Outline each uninfected red blood cell.
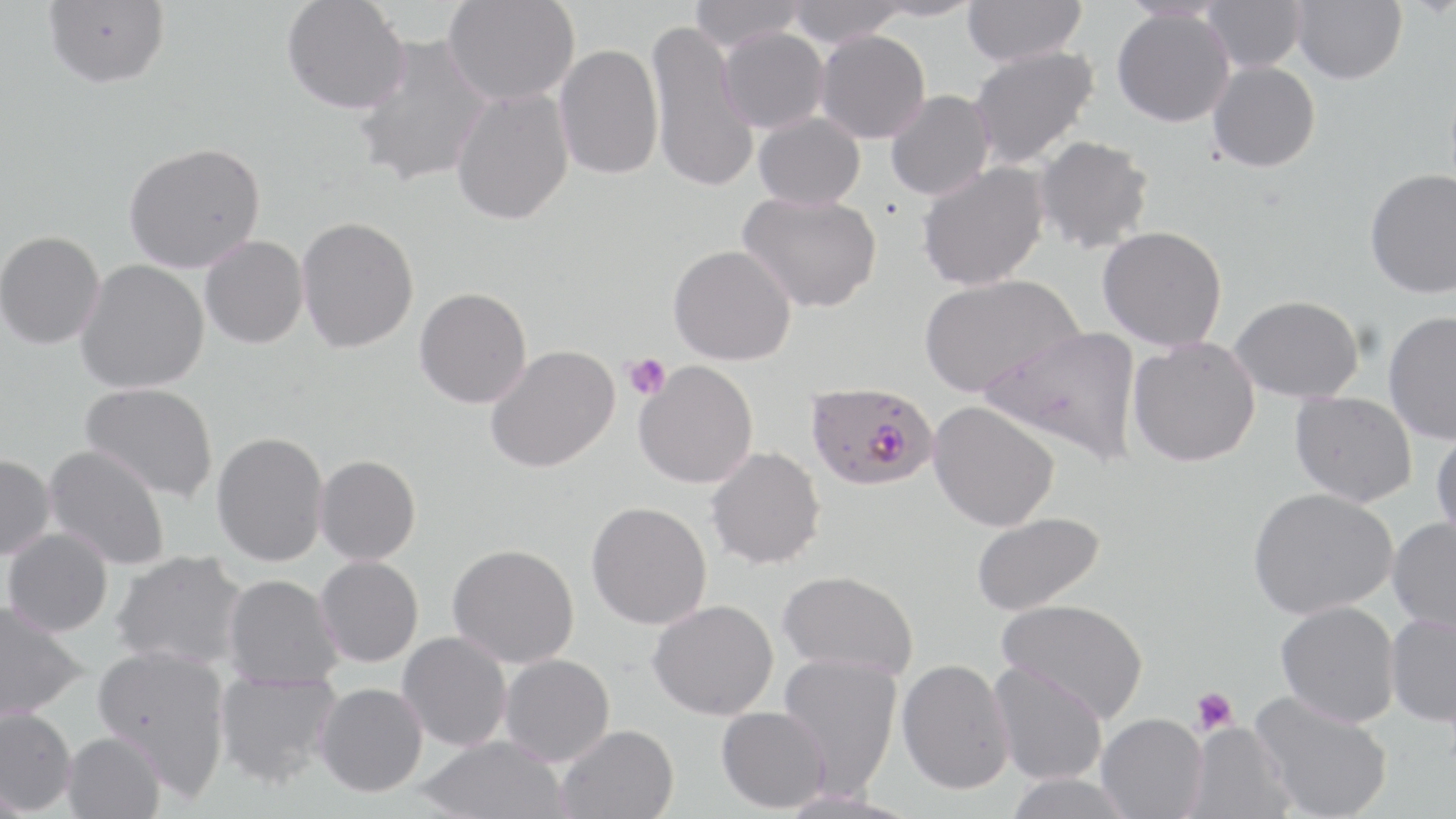
Approximate bounding boxes as (x1, y1, x2, y2) in pixels.
Uninfected red blood cells: (281, 0, 409, 117), (442, 0, 579, 107), (689, 0, 806, 52), (786, 0, 907, 47), (865, 0, 983, 22), (962, 0, 1087, 66), (1202, 0, 1306, 73), (1291, 0, 1407, 84), (42, 1, 170, 93), (1112, 7, 1235, 127), (645, 19, 760, 195), (718, 27, 829, 133), (815, 29, 931, 144), (351, 34, 494, 189), (554, 43, 663, 180), (968, 45, 1099, 169), (1207, 61, 1321, 173), (451, 86, 575, 226), (885, 90, 994, 200), (753, 112, 865, 210), (1033, 135, 1155, 254), (124, 143, 266, 273), (916, 162, 1050, 291), (1365, 169, 1456, 299), (737, 190, 882, 313), (296, 216, 419, 354), (1098, 225, 1228, 351), (0, 230, 104, 349), (200, 235, 309, 349), (668, 244, 797, 367), (76, 259, 209, 394), (918, 273, 1083, 399), (414, 287, 532, 408), (1229, 294, 1365, 403), (1383, 310, 1456, 445), (982, 325, 1144, 465), (1128, 337, 1260, 467), (485, 345, 620, 473), (634, 360, 758, 488), (80, 382, 219, 503), (1289, 391, 1417, 507), (928, 401, 1060, 532), (1430, 428, 1456, 544), (211, 431, 329, 566), (43, 444, 171, 571), (705, 446, 826, 569), (0, 454, 56, 560), (314, 454, 421, 565), (1248, 487, 1398, 620), (586, 501, 712, 630), (970, 511, 1106, 616), (1387, 516, 1456, 634), (3, 527, 113, 637), (448, 543, 580, 668), (110, 549, 248, 670), (315, 555, 424, 667), (779, 570, 919, 679), (223, 574, 342, 688), (997, 598, 1149, 724), (648, 599, 779, 720), (1276, 600, 1400, 727), (0, 601, 87, 721), (1385, 613, 1456, 725), (398, 631, 512, 751), (92, 644, 232, 797), (778, 652, 903, 799), (499, 654, 615, 767), (897, 658, 1015, 794), (988, 660, 1108, 785), (214, 670, 342, 788), (315, 682, 428, 797), (1250, 691, 1393, 819), (0, 706, 78, 814), (716, 706, 830, 813), (1096, 713, 1208, 819), (1184, 721, 1295, 819), (555, 724, 679, 819), (62, 731, 166, 819), (416, 735, 570, 819), (1003, 772, 1136, 819), (771, 788, 920, 818).

Summary:
  - Plasmodium falciparum-infected red blood cell locations: (806, 381, 938, 491)
  - Platelet locations: (624, 353, 671, 401), (1191, 687, 1237, 735)
  - Slide-level diagnosis: Plasmodium falciparum
  - Field of view: one of a larger specimen
  - Stain: May-Grünwald-Giemsa
  - Magnification: 1000x
  - Image size: 1456×819 pixels
  - Preparation: thin blood smear
  - Modality: optical microscopy